Classify this cell by malaria status.
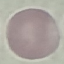

It is uninfected.

Summary:
  - Stain: Giemsa
  - Capture: smartphone camera at the microscope eyepiece
  - Preparation: thin blood smear
  - Image type: cell patch, automatically extracted from a larger field of view and resized to 64 × 64 pixels